Assess this cell for malaria.
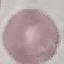

It is uninfected.

Summary:
  - Capture: smartphone camera at the microscope eyepiece
  - Stain: Giemsa
  - Image type: automatically extracted cell patch, resized to 64 × 64 pixels
  - Preparation: thin blood smear